State the blood parasite species.
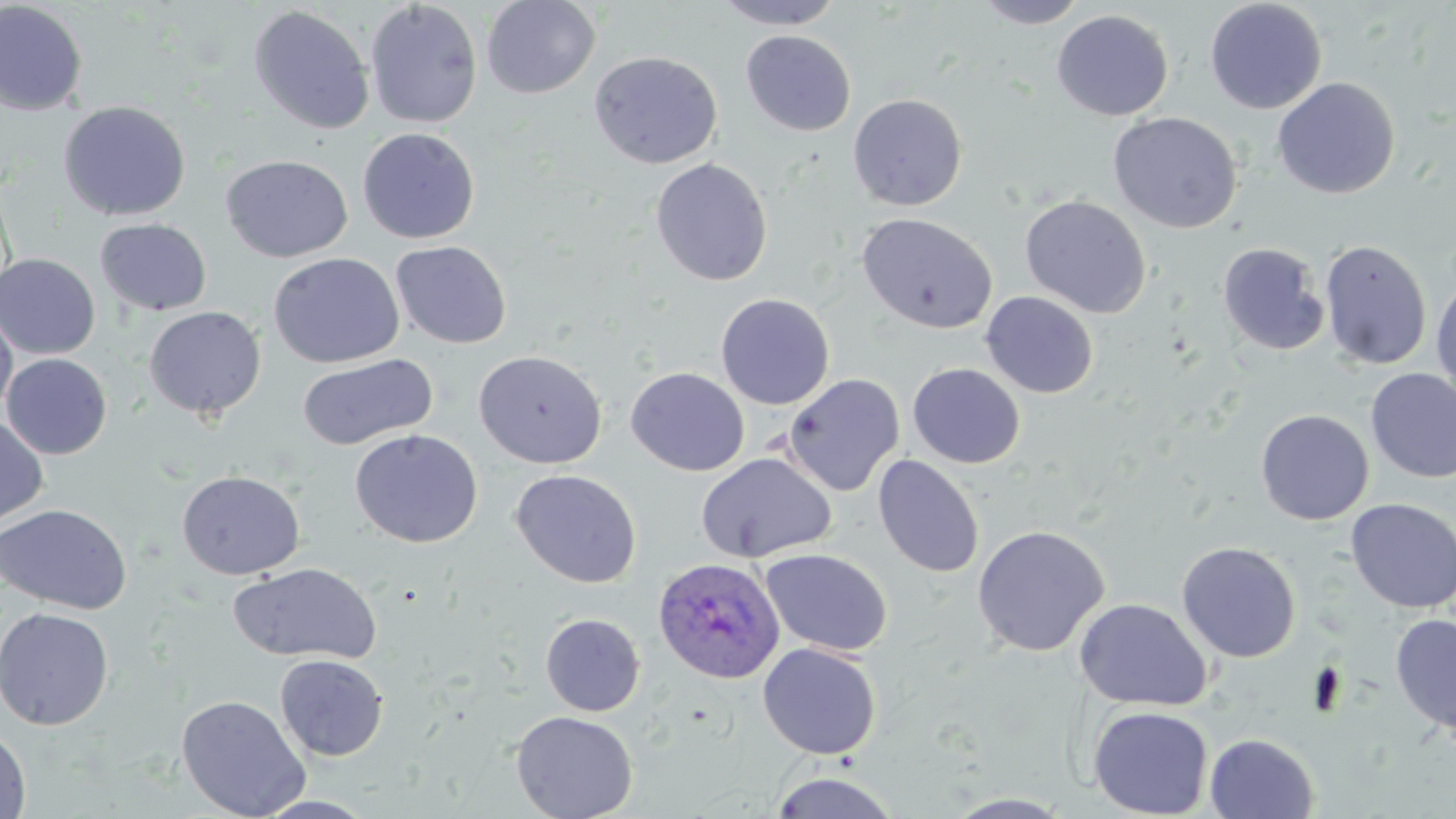
Plasmodium ovale.

{
  "uninfected_red_blood_cell_locations": "approximate bounding boxes as (x1, y1, x2, y2) in pixels: (364, 0, 483, 129), (481, 0, 600, 98), (712, 0, 846, 30), (973, 0, 1091, 29), (1204, 0, 1328, 115), (0, 2, 88, 116), (248, 5, 375, 136), (1051, 9, 1174, 121), (741, 30, 856, 136), (589, 51, 723, 169), (1272, 77, 1400, 200), (847, 93, 967, 211), (58, 100, 191, 221), (1108, 111, 1243, 234), (357, 127, 480, 244), (221, 154, 353, 263), (649, 158, 773, 286), (0, 178, 15, 306), (1020, 195, 1151, 318), (857, 212, 998, 334), (95, 218, 212, 317), (1318, 239, 1433, 370), (390, 241, 512, 349), (1217, 242, 1329, 356), (0, 252, 100, 359), (268, 252, 404, 369), (1431, 275, 1456, 405), (981, 291, 1099, 398), (715, 293, 835, 409), (0, 305, 18, 421), (143, 306, 266, 420), (474, 349, 608, 469), (2, 353, 112, 459), (298, 354, 438, 450), (907, 363, 1026, 469), (626, 367, 750, 476), (1365, 369, 1456, 484), (782, 373, 905, 496), (1255, 408, 1374, 525), (0, 414, 48, 529), (349, 428, 484, 548), (695, 452, 837, 563), (873, 454, 985, 578), (510, 469, 642, 588), (176, 470, 305, 580), (1345, 498, 1456, 613), (0, 504, 132, 615), (971, 524, 1109, 657), (1177, 541, 1301, 663), (760, 548, 893, 656), (229, 562, 383, 665), (1074, 598, 1212, 711), (0, 607, 115, 730), (540, 613, 646, 716), (1390, 613, 1456, 737), (757, 641, 883, 760), (275, 654, 389, 761), (176, 694, 311, 819), (1088, 706, 1213, 818), (511, 710, 639, 819), (0, 725, 32, 819), (1204, 732, 1319, 818), (767, 771, 902, 818), (943, 792, 1075, 817), (253, 794, 380, 818)",
  "magnification": "1000x",
  "field_of_view": "single",
  "modality": "light microscopy",
  "plasmodium_ovale_infected_red_blood_cell_locations": "approximate bounding boxes as (x1, y1, x2, y2) in pixels: (652, 557, 785, 685)",
  "stain": "May-Grünwald-Giemsa",
  "preparation": "thin blood film",
  "image_size": "1456×819 pixels"
}